Assess this cell for malaria.
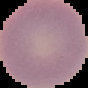

Uninfected.

Summary:
  - Image size: 88×88 pixels
  - Image type: segmented cell region with the area outside set to black
  - Preparation: thin blood film